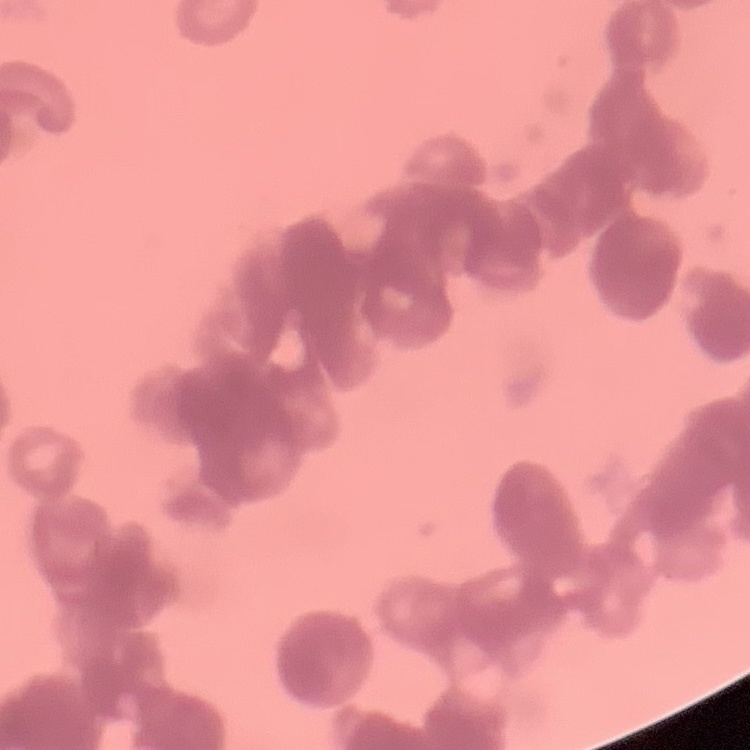
The red blood cells show rouleaux formation. Thin blood film. Stained with either Field's or Giemsa. Square crop of a larger photomicrograph.